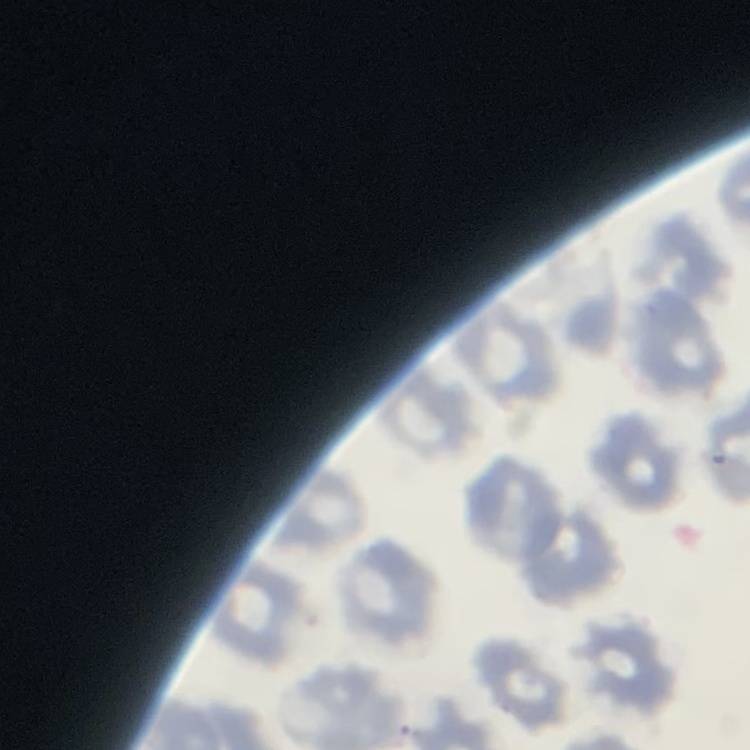
{
  "erythrocyte_morphology": "no rouleaux formation",
  "image_type": "square crop of a larger photomicrograph",
  "stain": "Field's or Giemsa",
  "preparation": "thin peripheral smear"
}